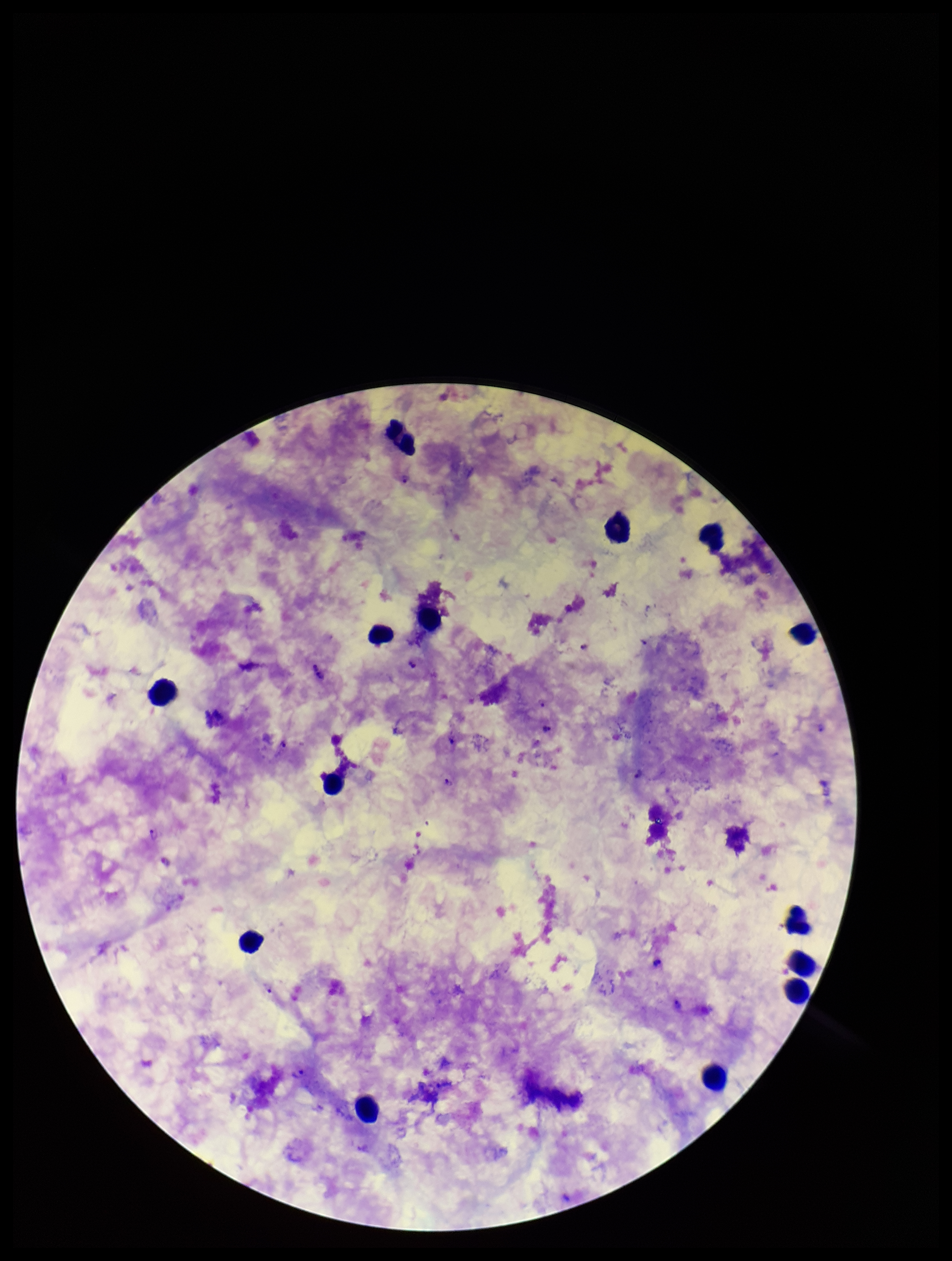
leukocyte_count: 14
plasmodium_parasites: seen
species_reported_for_this_patient: Plasmodium falciparum
image_size: 952×1261 pixels
field_of_view: one from this slide
parasite_count: 12
stain: Giemsa
patient_malaria_status: infected
preparation: thick
capture: smartphone photograph through the microscope eyepiece